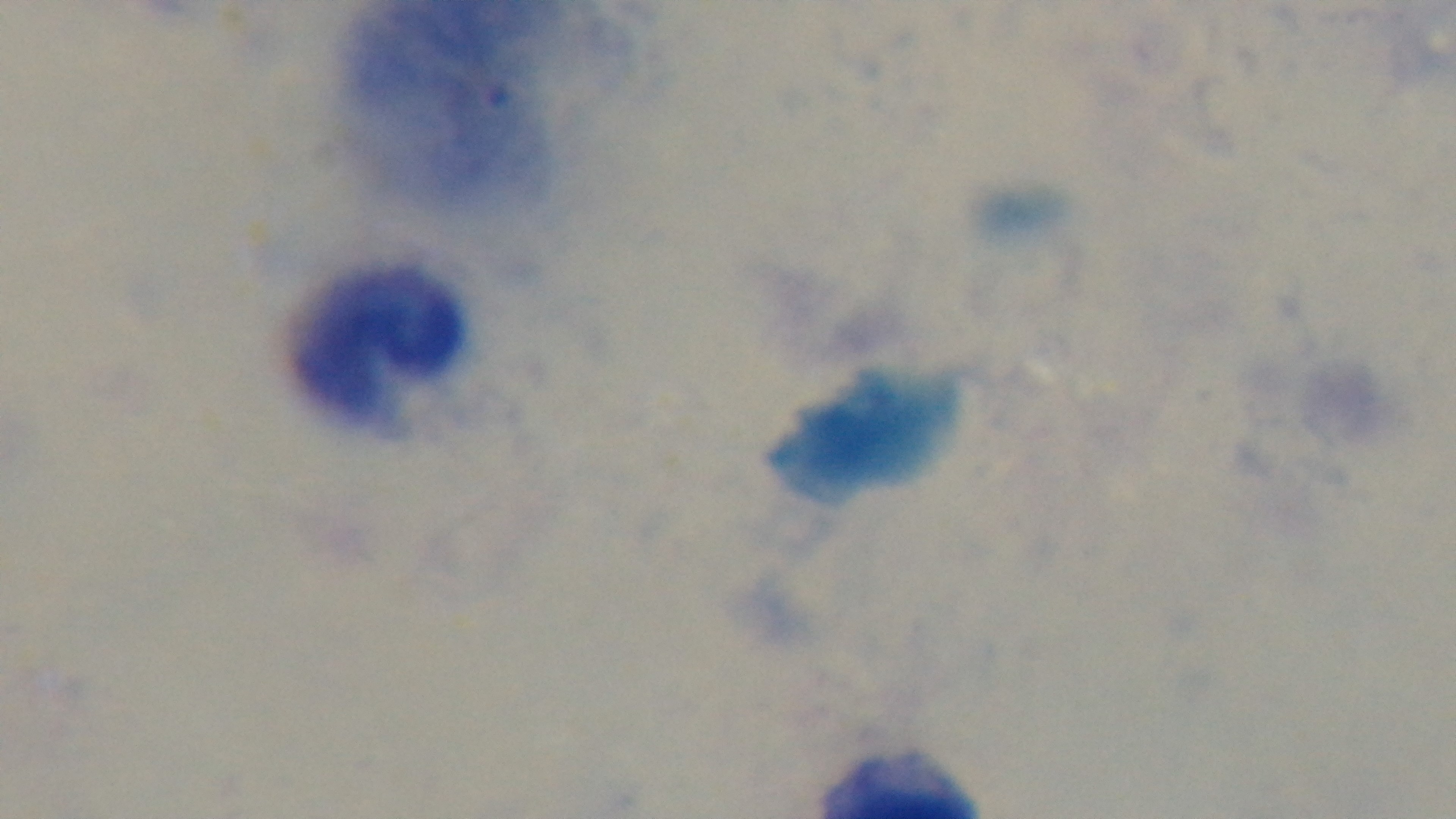 Captured with a mounted 4K digital camera. One field from the slide. Photomicrograph. Giemsa-stained. Preparation: thick smear. 100x oil-immersion objective. Malaria status: negative.